Report the malaria status.
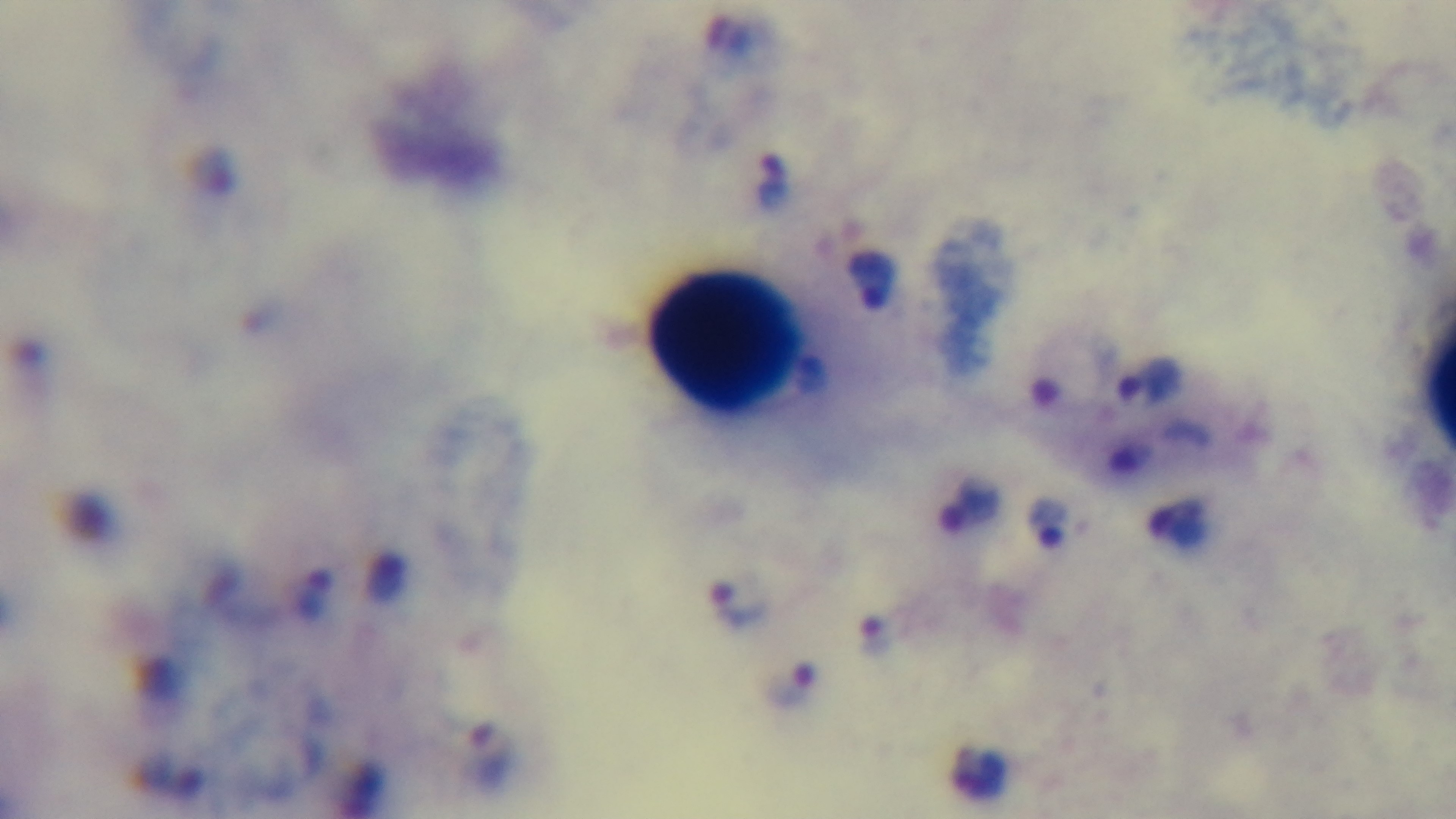

It is infected.

modality = light microscopy
objective = 100x oil immersion
preparation = thick
capture = mounted 4K digital camera
stain = Giemsa
field of view = one from the slide